Classify this cell by malaria status.
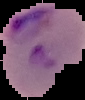

It is parasitized.

Summary:
  - Preparation: thin blood film
  - Image size: 85×100 pixels
  - Image type: segmented cell region on a black background